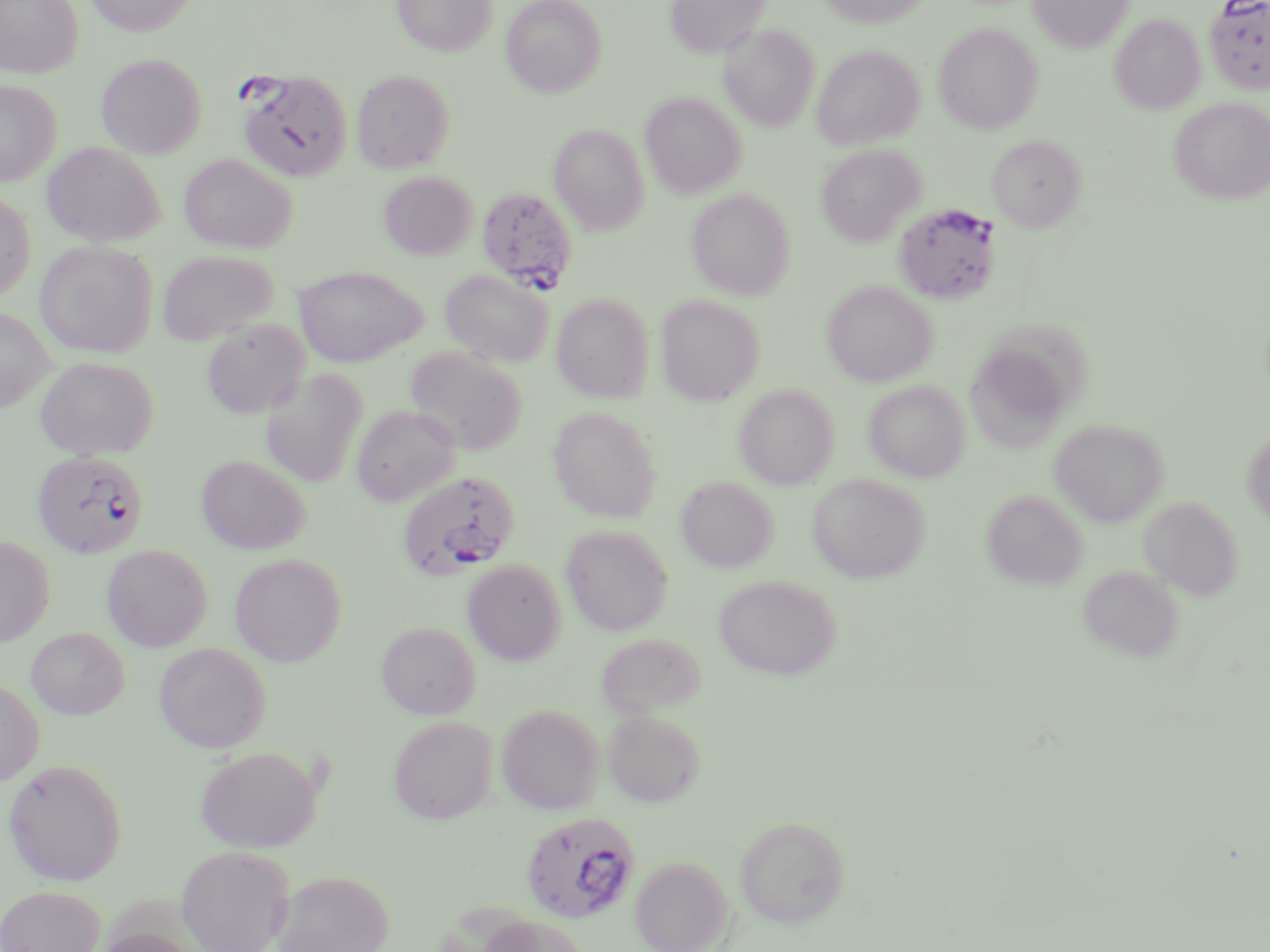
Summary:
  - Coordinate format: approximate bounding boxes as (x1,y1)-(x2,y2) corner pairs in pixels
  - Plasmodium falciparum-infected red blood cell locations: (1204,0)-(1270,95), (237,69)-(354,182), (476,186)-(578,295), (894,202)-(1000,305), (32,450)-(149,558), (397,470)-(519,582), (520,811)-(641,924)
  - Uninfected red blood cell locations: (0,0)-(84,78), (84,0)-(197,36), (392,0)-(496,56), (501,0)-(607,97), (664,0)-(770,57), (818,0)-(933,28), (1027,0)-(1134,53), (1110,14)-(1205,114), (719,23)-(820,131), (933,23)-(1043,134), (812,44)-(925,150), (96,54)-(206,158), (351,70)-(454,173), (0,79)-(61,186), (640,92)-(746,199), (1168,97)-(1270,204), (549,124)-(649,234), (990,135)-(1089,232), (41,142)-(166,248), (816,143)-(925,246), (179,154)-(297,253), (378,171)-(478,260), (687,189)-(795,300), (0,191)-(36,301), (35,240)-(157,358), (156,249)-(278,346), (293,265)-(427,367), (441,269)-(552,368), (823,280)-(937,386), (552,293)-(653,403), (656,294)-(765,405), (0,306)-(54,413), (990,313)-(1097,413), (201,319)-(310,419), (405,346)-(528,456), (967,347)-(1065,456), (35,356)-(159,460), (260,369)-(368,488), (863,380)-(971,482), (734,385)-(839,489), (351,404)-(461,507), (547,406)-(663,522), (1049,419)-(1169,527), (1242,428)-(1270,529), (196,455)-(311,555), (807,473)-(930,583), (676,475)-(777,572), (982,488)-(1088,590), (1138,496)-(1243,601), (560,525)-(673,636), (0,536)-(55,646), (103,544)-(212,651), (230,553)-(347,666), (462,559)-(566,665), (1078,564)-(1185,663), (714,574)-(841,680), (376,621)-(480,719), (26,627)-(129,719), (595,632)-(706,719), (154,642)-(272,753), (0,677)-(45,786), (496,703)-(604,814), (602,709)-(706,807), (388,715)-(498,824), (195,746)-(322,853), (3,758)-(128,886), (735,817)-(849,927), (177,845)-(295,952), (630,856)-(734,952), (273,869)-(395,952), (0,885)-(105,952), (478,914)-(589,952), (95,928)-(200,952)
  - Slide-level diagnosis: Plasmodium falciparum
  - Image size: 1270×952 pixels
  - Field of view: one of a larger specimen
  - Magnification: 1000x
  - Modality: optical microscopy
  - Stain: May-Grünwald-Giemsa
  - Preparation: thin blood film